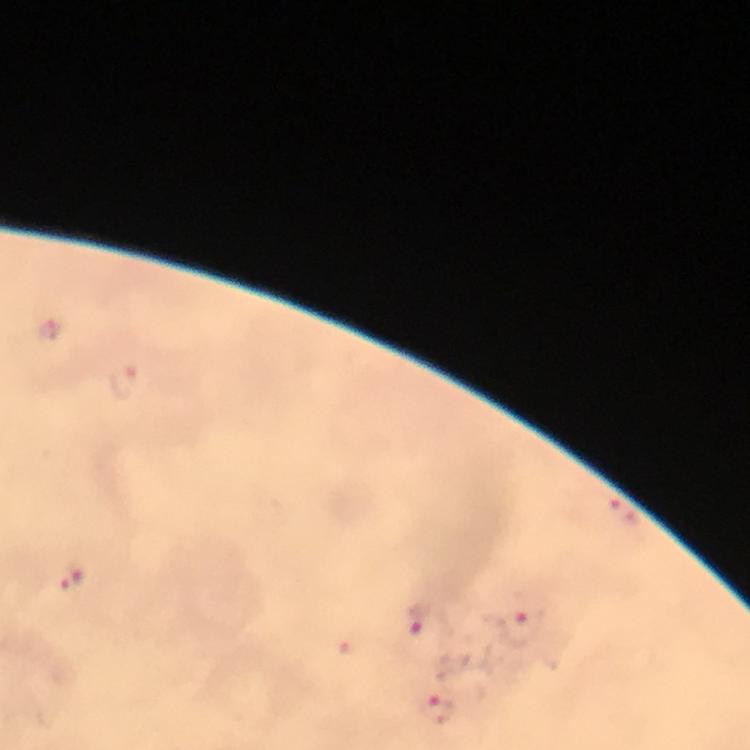

{
  "image_size": "750×750 pixels",
  "capture": "smartphone camera through the microscope",
  "plasmodium_parasite_locations": "approximate centers as [x, y] in pixels: [123, 379], [624, 508], [73, 578], [419, 618], [519, 627], [436, 708]",
  "magnification": "100x",
  "preparation": "thick blood film",
  "cropped_from": "one field of view",
  "stain": "Giemsa",
  "immersion_oil": "used",
  "context": "from a malaria diagnostic workup"
}